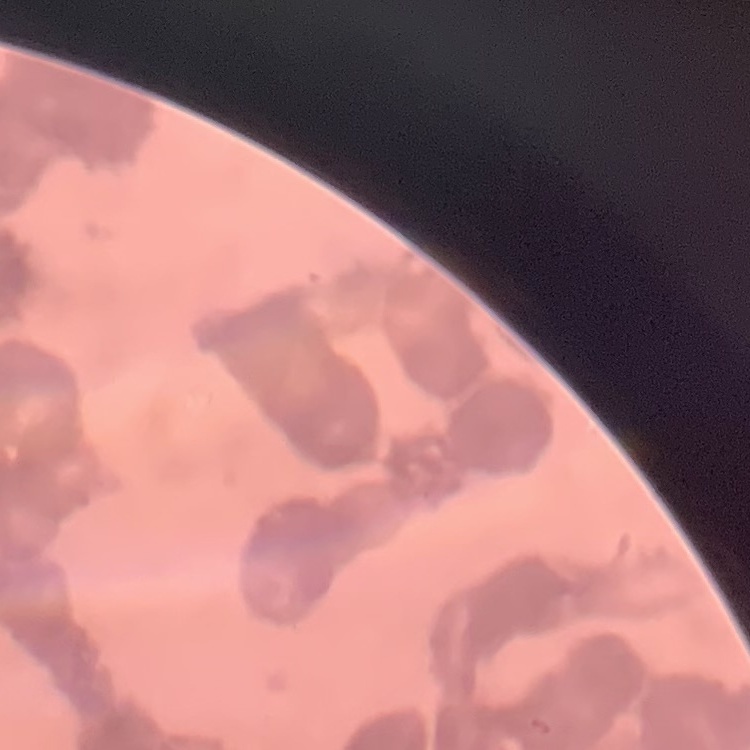 The erythrocytes exhibit rouleaux formation. Thin blood film. Square crop of a larger photomicrograph. Field's or Giemsa stain.